Assess this cell for malaria.
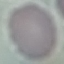

Uninfected.

Summary:
  - Capture: smartphone camera at the microscope eyepiece
  - Stain: Giemsa
  - Preparation: thin blood film
  - Image type: cell patch, automatically extracted from a larger field of view and resized to 64 × 64 pixels